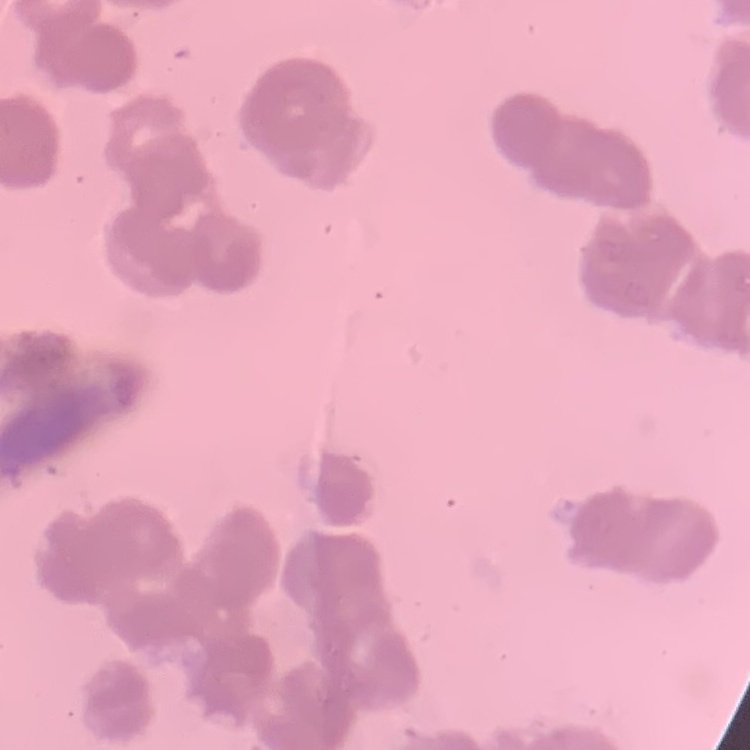

Summary:
  - Red blood cell morphology: rouleaux formation
  - Stain: Field's or Giemsa
  - Preparation: thin blood smear
  - Image type: square crop of a larger photomicrograph